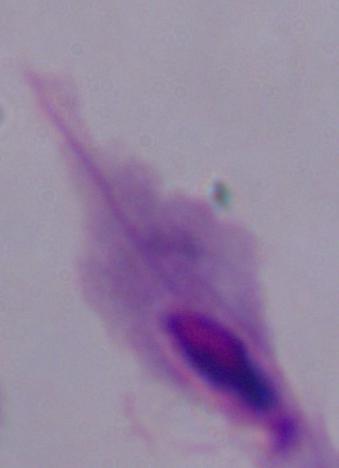
modality = micrograph
magnification = 1000x
identification = trichomonad